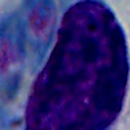

magnification = 1000x
identification = white blood cell
modality = photomicrograph